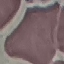
result: negative for malaria parasites
stain: Giemsa
preparation: thin blood film
capture: smartphone camera at the microscope eyepiece
image_type: automatically extracted cell patch, resized to 64 × 64 pixels